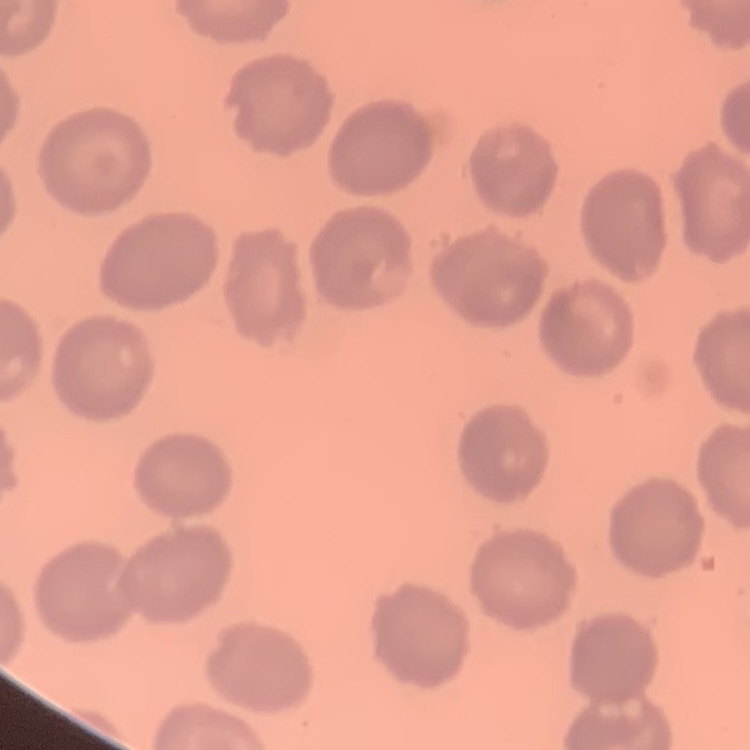
erythrocyte_morphology: no rouleaux formation
image_type: one tile cut from a larger photomicrograph
preparation: thin blood smear
stain: Field's or Giemsa